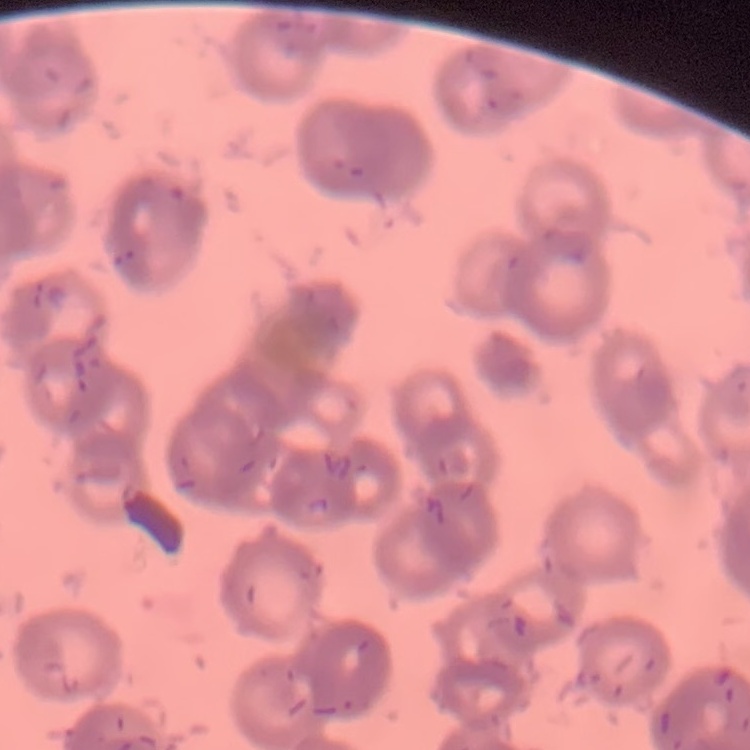

Summary:
  - Red blood cell morphology: rouleaux formation
  - Image type: one tile cut from a larger photomicrograph
  - Preparation: thin blood film
  - Stain: Field's or Giemsa